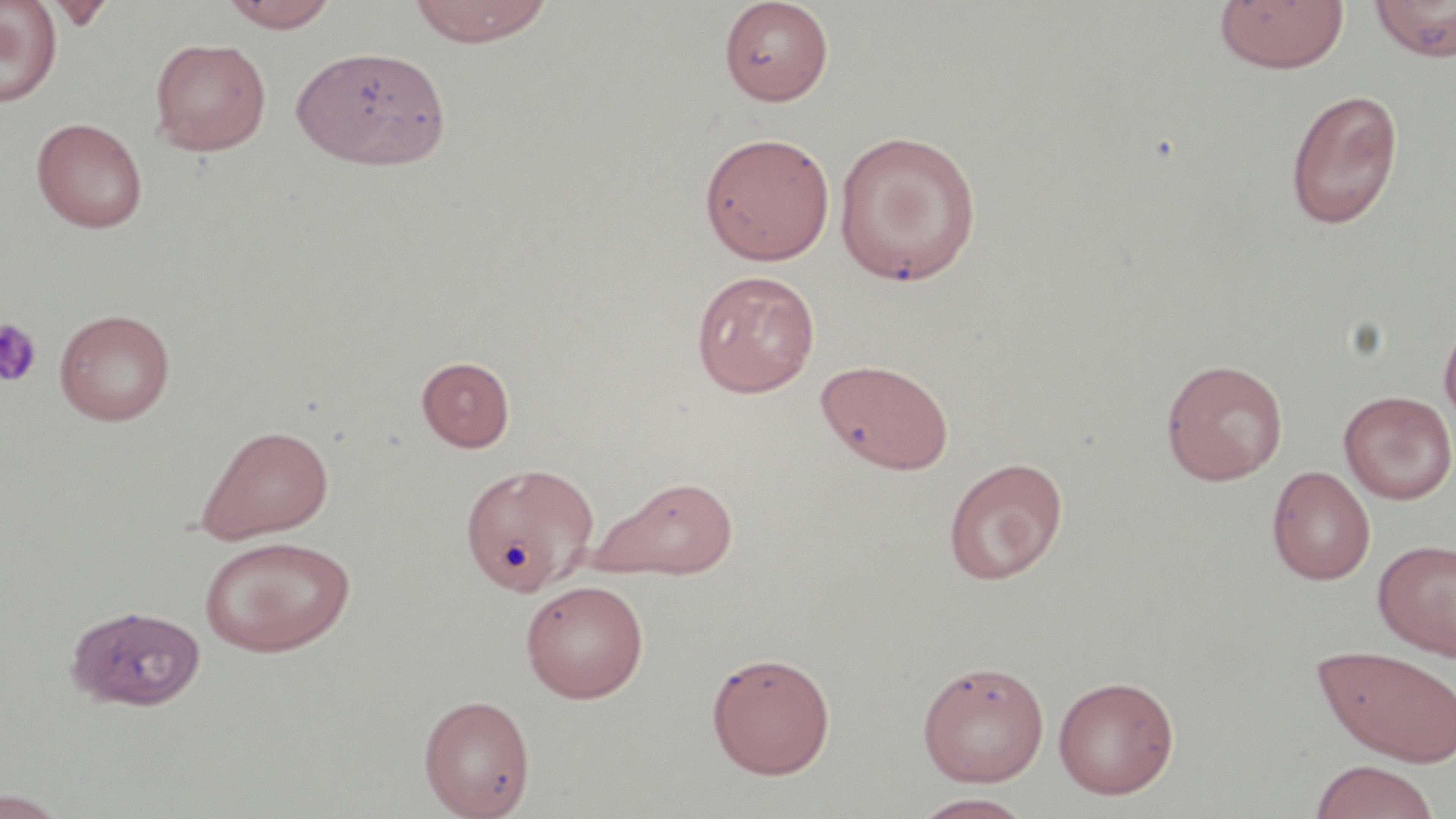
slide-level diagnosis = no evidence of blood parasites
magnification = 1000x
stain = May-Grünwald-Giemsa
image size = 1456×819 pixels
platelet locations = approximate bounding boxes as (x1, y1, x2, y2) in pixels: (0, 317, 43, 388)
preparation = thin blood film
field of view = single
uninfected red blood cell locations = approximate bounding boxes as (x1, y1, x2, y2) in pixels: (0, 0, 62, 107), (220, 0, 340, 31), (406, 0, 556, 47), (1369, 0, 1456, 61), (45, 1, 115, 31), (719, 1, 834, 106), (1214, 1, 1349, 74), (150, 37, 271, 156), (291, 45, 451, 172), (1285, 88, 1404, 230), (32, 117, 148, 233), (833, 130, 982, 285), (698, 131, 835, 265), (691, 269, 820, 398), (54, 308, 175, 426), (1438, 311, 1456, 434), (417, 356, 515, 451), (815, 358, 954, 474), (1161, 358, 1289, 486), (1338, 390, 1456, 505), (196, 424, 334, 543), (943, 456, 1068, 585), (459, 461, 600, 596), (1266, 465, 1375, 585), (593, 476, 739, 579), (199, 534, 355, 657), (1373, 538, 1456, 659), (520, 579, 649, 703), (65, 605, 213, 719), (1313, 645, 1456, 767), (705, 650, 836, 779), (916, 660, 1050, 786), (1052, 675, 1179, 799), (418, 694, 535, 818), (1309, 760, 1441, 819), (0, 789, 73, 819), (911, 792, 1036, 818)
modality = optical microscopy